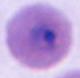
Summary:
  - Modality: photomicrograph
  - Identification: Plasmodium
  - Magnification: 400x or 1000x